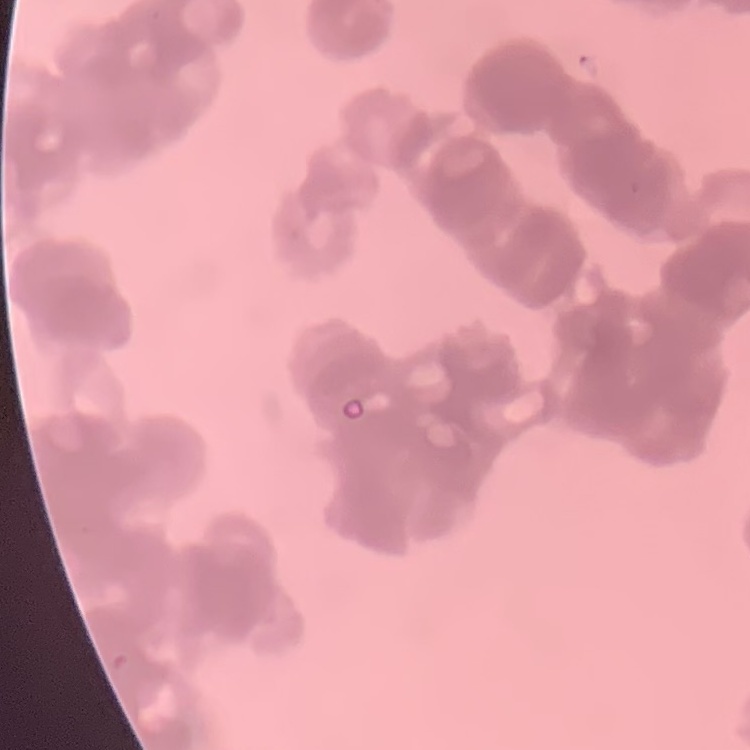 The erythrocytes show rouleaux formation. Square crop of a larger photomicrograph. Thin blood smear. Stained with either Field's or Giemsa.